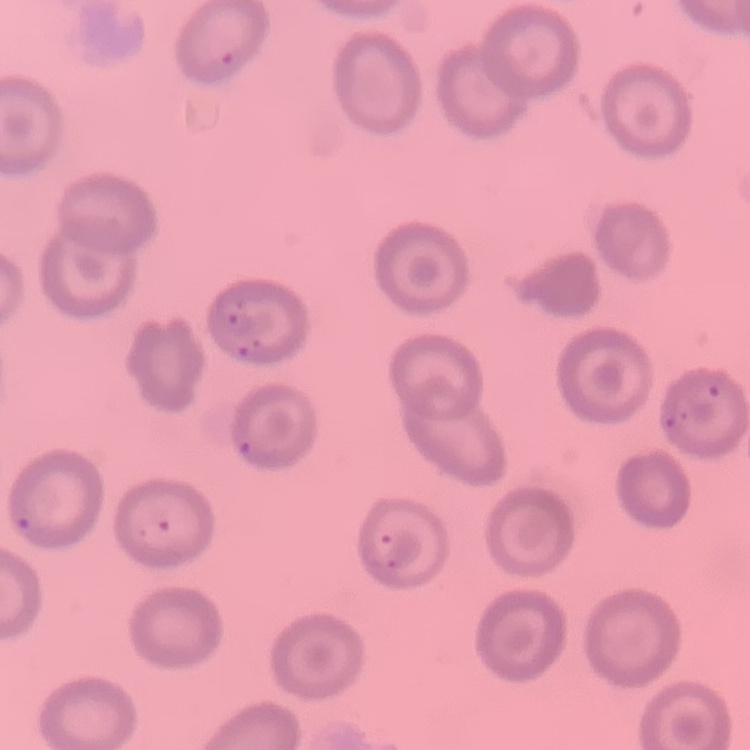
The erythrocytes exhibit no rouleaux formation. Square crop of a larger photomicrograph. Field's or Giemsa stain. Thin blood smear.